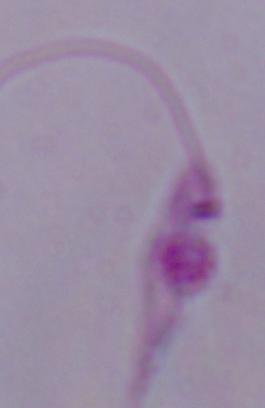

magnification = 1000x
modality = micrograph
identification = Leishmania